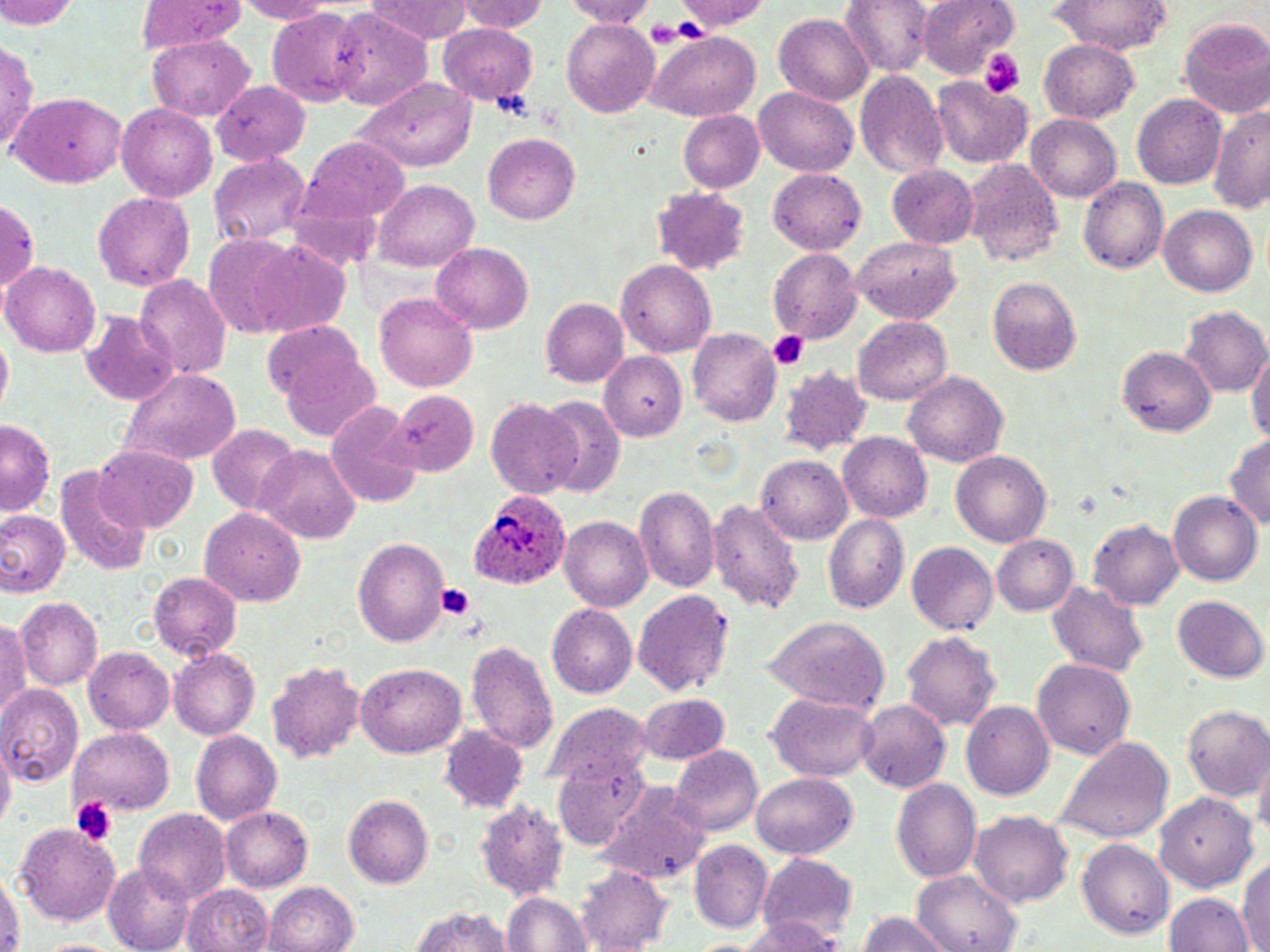
plasmodium_ovale_infected_red_blood_cell_locations: 'approximate bounding boxes as (x1,y1)-(x2,y2) corner pairs in pixels: (465,487)-(571,590)'
slide_level_diagnosis: Plasmodium ovale
field_of_view: single
platelet_locations: 'approximate bounding boxes as (x1,y1)-(x2,y2) corner pairs in pixels: (645,20)-(685,46), (980,48)-(1026,99), (489,86)-(537,123), (768,331)-(811,371), (434,582)-(479,620), (69,794)-(120,849)'
uninfected_red_blood_cell_locations: 'approximate bounding boxes as (x1,y1)-(x2,y2) corner pairs in pixels: (0,0)-(80,31), (137,0)-(246,53), (228,0)-(335,22), (366,0)-(473,43), (459,0)-(546,34), (558,0)-(663,24), (679,0)-(771,34), (840,0)-(933,77), (918,0)-(1018,80), (1048,1)-(1175,54), (328,9)-(432,108), (267,10)-(363,107), (771,12)-(875,106), (1177,17)-(1270,118), (561,20)-(661,117), (437,24)-(539,104), (644,32)-(760,119), (147,35)-(253,121), (1039,37)-(1140,122), (0,40)-(39,158), (854,70)-(949,180), (931,75)-(1030,167), (356,76)-(479,172), (214,77)-(312,164), (755,85)-(860,176), (13,92)-(126,187), (1133,95)-(1225,188), (117,104)-(215,202), (1209,107)-(1270,216), (676,110)-(765,194), (1025,113)-(1121,201), (485,134)-(581,224), (300,140)-(410,230), (209,152)-(311,249), (963,157)-(1064,267), (886,165)-(976,246), (766,170)-(865,255), (1079,177)-(1169,275), (376,178)-(481,270), (651,185)-(754,274), (93,193)-(197,290), (0,198)-(41,296), (1158,204)-(1257,295), (201,234)-(299,333), (848,236)-(963,322), (431,240)-(535,333), (237,241)-(353,336), (770,249)-(862,345), (615,258)-(716,356), (5,260)-(101,356), (136,276)-(231,381), (989,277)-(1083,377), (375,290)-(479,394), (541,298)-(628,387), (1181,306)-(1269,398), (81,312)-(180,407), (853,317)-(953,406), (265,320)-(375,421), (688,325)-(780,426), (1248,341)-(1270,450), (1118,345)-(1213,436), (597,349)-(687,439), (779,364)-(870,454), (116,368)-(243,467), (905,371)-(1008,467), (389,391)-(479,476), (537,395)-(624,497), (486,401)-(584,500), (327,403)-(422,506), (0,423)-(55,515), (207,425)-(301,514), (836,434)-(931,522), (1225,434)-(1270,535), (90,446)-(198,533), (255,446)-(362,543), (951,450)-(1053,547), (757,455)-(854,543), (57,464)-(151,577), (634,487)-(720,595), (1168,489)-(1262,588), (708,496)-(805,613), (198,508)-(306,607), (0,510)-(68,597), (823,512)-(909,612), (560,516)-(652,610), (1089,517)-(1183,606), (993,534)-(1079,617), (353,538)-(448,646), (907,544)-(997,634), (147,570)-(241,661), (1046,580)-(1147,676), (634,590)-(734,698), (1171,594)-(1267,683), (15,597)-(104,687), (547,605)-(638,698), (764,615)-(888,714), (0,618)-(30,721), (902,633)-(1001,732), (465,639)-(559,756), (84,647)-(174,735), (169,649)-(259,740), (265,659)-(366,761), (1032,660)-(1137,759), (354,662)-(466,758), (0,681)-(85,785), (766,692)-(877,782), (637,694)-(730,764), (546,700)-(648,783), (857,702)-(950,792), (962,702)-(1053,801), (1182,706)-(1270,803), (70,727)-(174,812), (440,727)-(529,813), (191,732)-(281,825), (1056,735)-(1173,847), (671,746)-(761,836), (1,747)-(14,832), (1253,753)-(1269,847), (751,772)-(858,860), (892,778)-(982,884), (598,785)-(711,884), (1155,791)-(1258,892), (343,795)-(432,887), (476,799)-(567,897), (221,806)-(312,892), (134,809)-(230,903), (971,812)-(1073,907), (15,820)-(120,924), (1077,839)-(1174,939), (690,840)-(774,930), (756,853)-(857,943), (1238,858)-(1269,952), (104,861)-(195,952), (579,864)-(672,951), (0,870)-(20,952), (910,870)-(1025,952), (263,881)-(360,952), (184,882)-(271,952), (500,890)-(595,952), (1168,894)-(1252,952), (410,905)-(512,952), (856,911)-(952,952), (734,916)-(838,952), (40,937)-(120,952)'
modality: light microscopy
image_size: 1270×952 pixels
stain: May-Grünwald-Giemsa
magnification: 1000x
preparation: thin blood film